Report the malaria status of this cell.
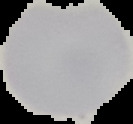
Uninfected.

From a thin blood film. Image is 133×124 pixels. The area outside the segmented cell region is set to black.